Comment on the morphology of the red blood cells.
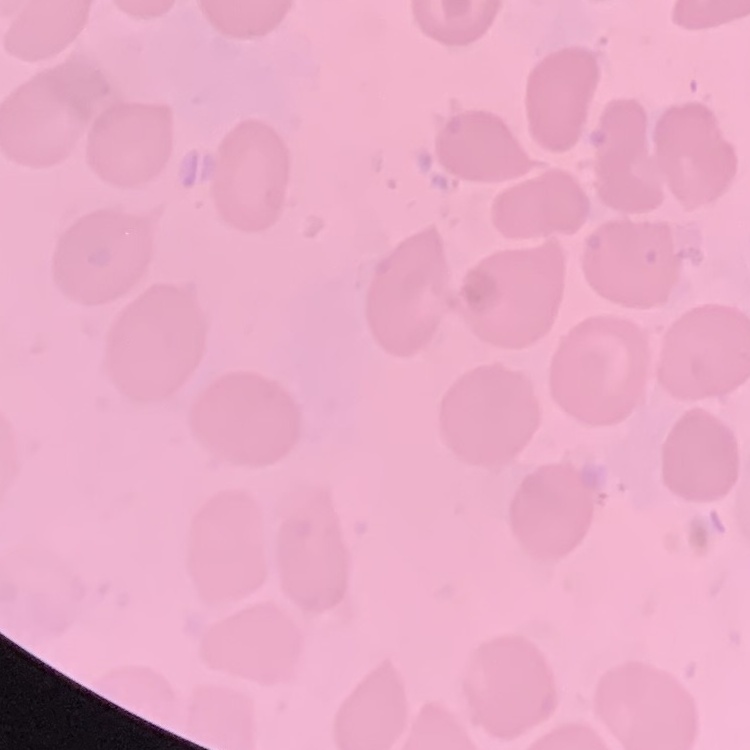
They show no rouleaux formation.

image type = one tile cut from a larger photomicrograph
stain = Field's or Giemsa
preparation = thin blood film